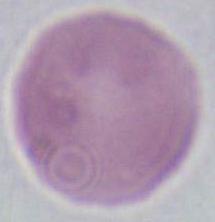

1000x magnification. Photomicrograph. A red blood cell is seen.